Assess for Plasmodium parasites.
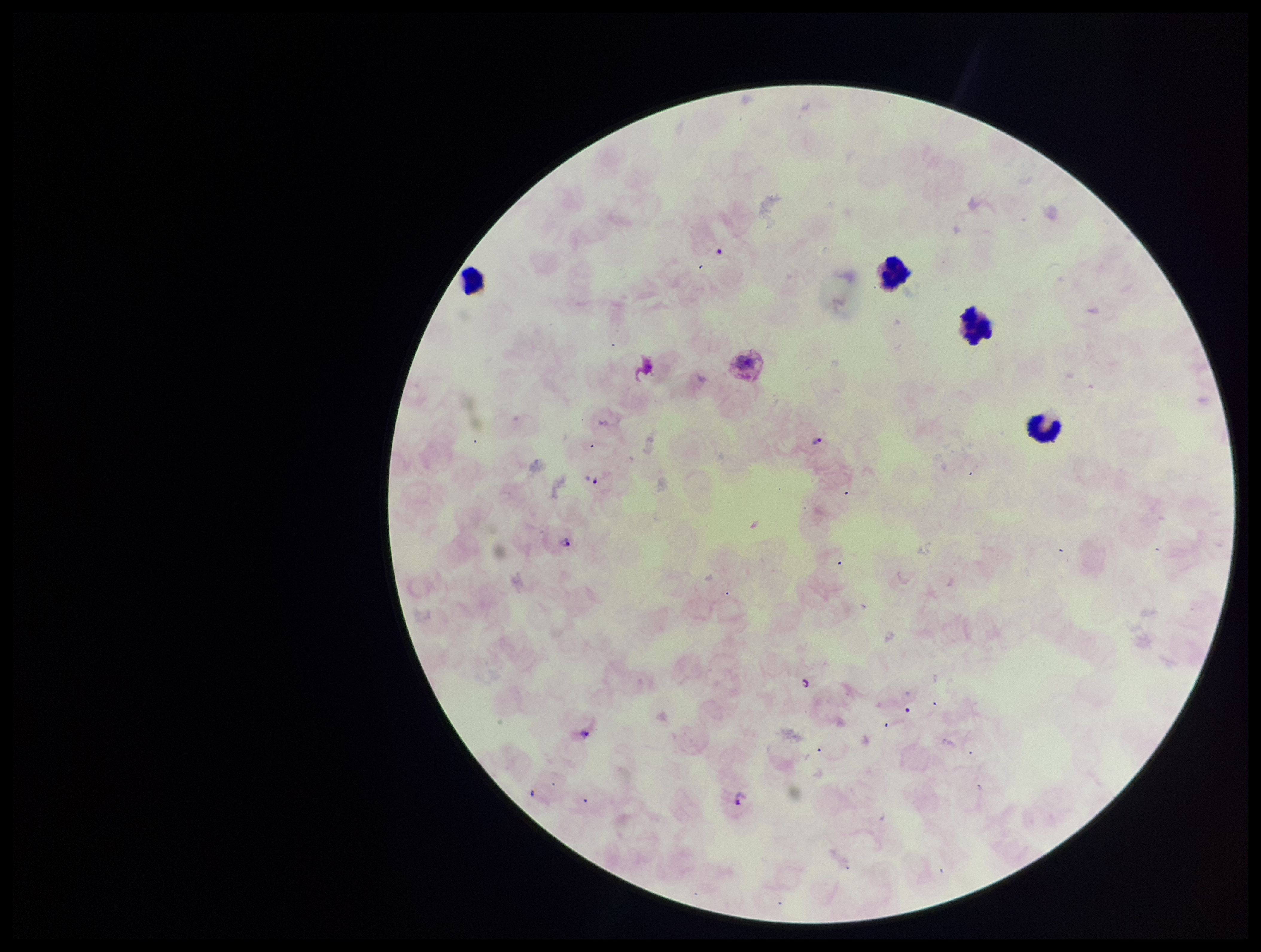
Detected.

Summary:
  - Stain: Giemsa
  - Parasite count: 5
  - Leukocyte count: 4
  - Species reported for this patient: Plasmodium vivax
  - Patient malaria status: positive
  - Preparation: thick blood smear
  - Field of view: one from this slide
  - Capture: smartphone photograph through the microscope eyepiece
  - Image size: 1261×952 pixels